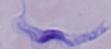

Photomicrograph. A trypanosome is seen. 1000x magnification.